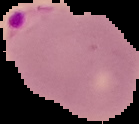
preparation = thin blood smear
image type = cell region segmented out of the field of view; surrounding area masked to black
result = malaria parasites detected
image size = 139×124 pixels